Identify the cell.
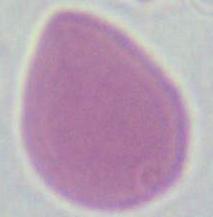

This is an erythrocyte.

Summary:
  - Magnification: 1000x
  - Modality: micrograph